Report the malaria status.
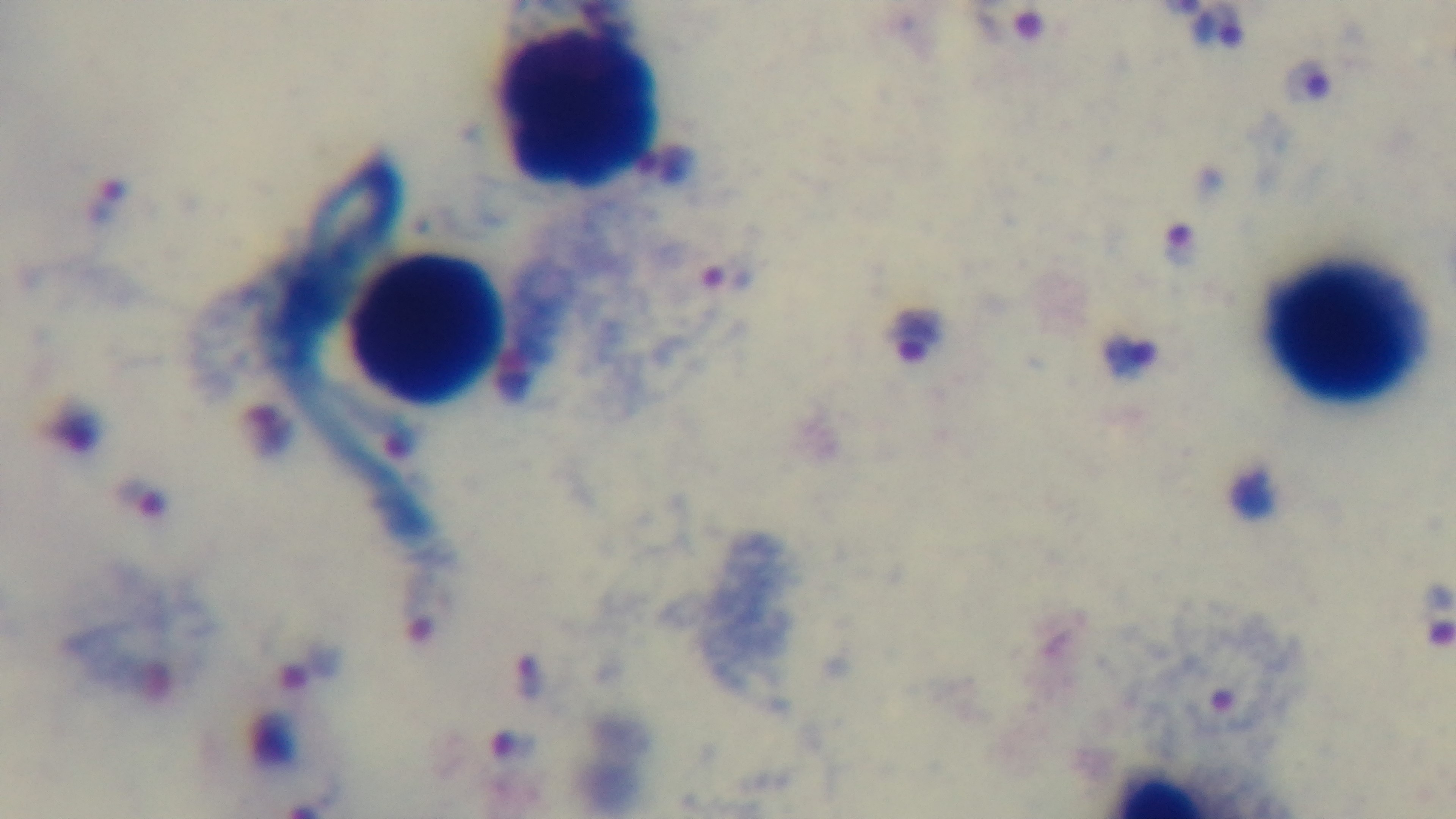
It is infected.

Captured with a mounted 4K digital camera. Preparation: thick blood film. 100x oil-immersion objective. Giemsa stain. Photomicrograph. One field from the slide.